Classify this cell by malaria status.
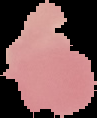
Uninfected.

image type = cell region segmented out of the field of view; surrounding area masked to black
preparation = thin blood film
image size = 97×118 pixels